Give the position of each P. falciparum parasite with its life-cycle stage, each leukocyte, and any debris.
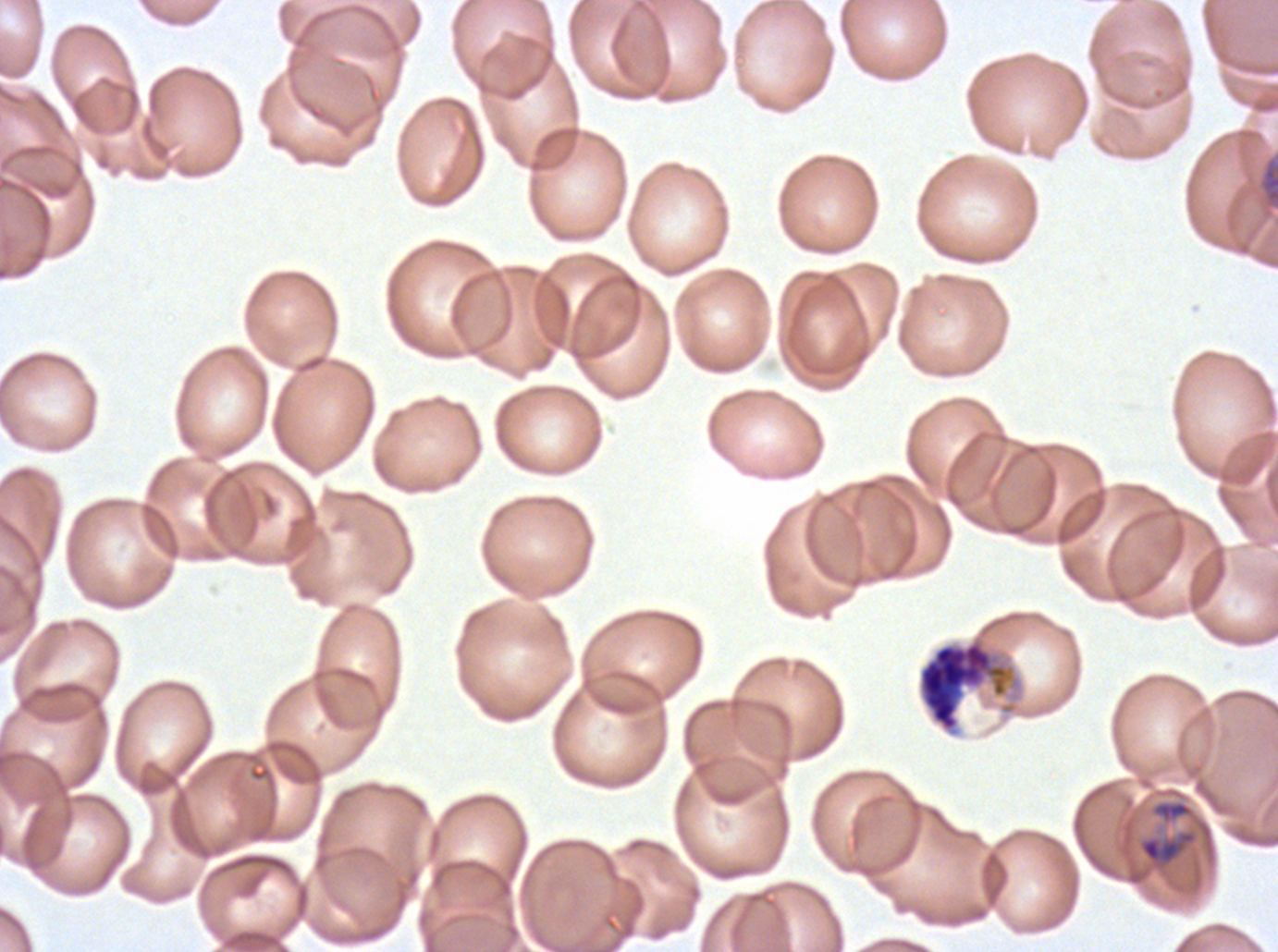
Approximate bounding boxes as (x1, y1, x2, y2) in pixels.
Late schizonts: (1256, 150, 1277, 218), (917, 635, 1023, 735).
Debris: (1137, 829, 1198, 870).
No rings, late-ring/early-trophozoite forms, mid trophozoites, late trophozoites, early schizonts, segmenters, gametocytes, or leukocytes observed.

Image is 1278×952 pixels. Ex-vivo P. falciparum culture from a patient in The Gambia, grown for 24 to 48 hours. Giemsa stain. Thin blood film. A sub-image separated from a larger composite.